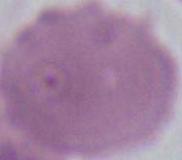

Summary:
  - Identification: red blood cell
  - Magnification: 1000x
  - Modality: micrograph